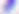

magnification: 400x
modality: photomicrograph
identification: Toxoplasma gondii